Point out each Plasmodium parasite.
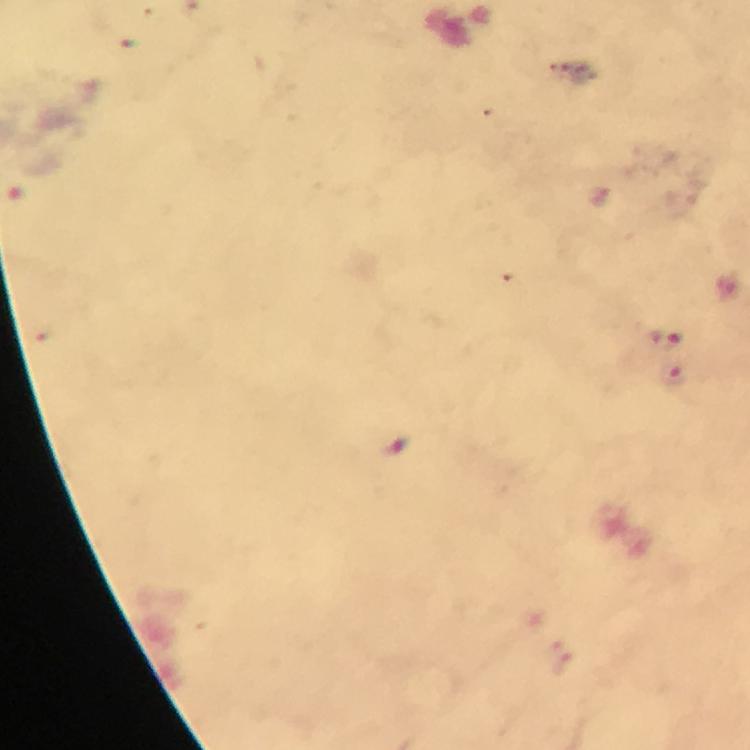
Approximate centers as {x, y} in pixels.
Plasmodium parasites: {667, 340}, {675, 375}.

{
  "cropped_from": "one field of view",
  "capture": "smartphone mounted on the microscope",
  "image_size": "750×750 pixels",
  "context": "from a malaria diagnostic workup",
  "immersion_oil": "applied",
  "stain": "Giemsa",
  "magnification": "100x",
  "preparation": "thick smear"
}